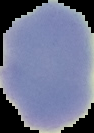

Summary:
  - Image size: 94×133 pixels
  - Image type: segmented cell region with the area outside set to black
  - Preparation: thin blood film
  - Malaria status: uninfected